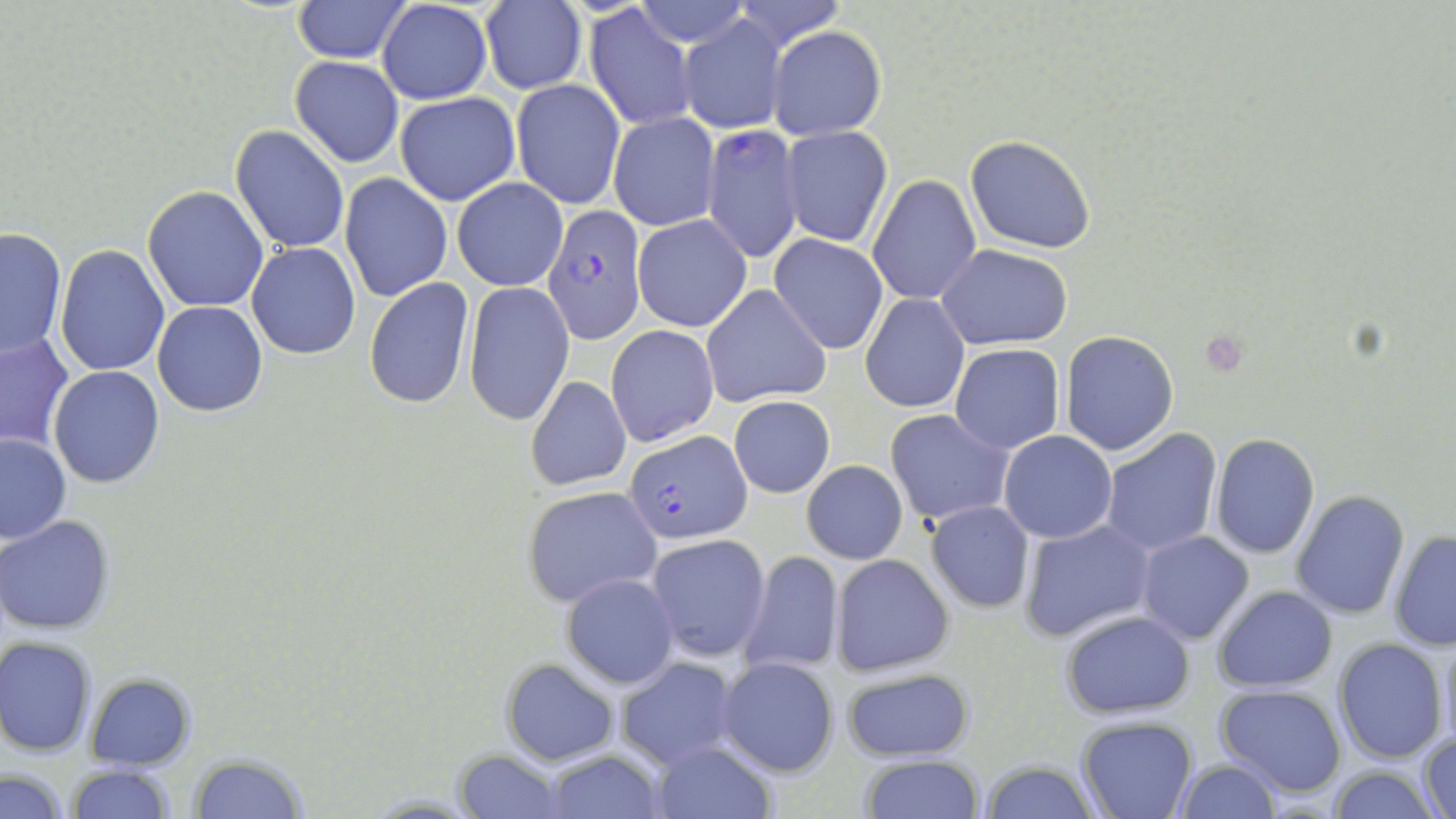
Summary:
  - Coordinate format: approximate bounding boxes as [x1, y1, x2, y2] in pixels
  - Plasmodium falciparum-infected red blood cell locations: [702, 124, 803, 262], [543, 207, 646, 340], [625, 432, 751, 543]
  - Uninfected red blood cell locations: [732, 0, 846, 52], [294, 1, 406, 62], [377, 1, 493, 104], [632, 1, 752, 47], [480, 2, 586, 94], [584, 5, 698, 131], [678, 16, 788, 133], [768, 26, 888, 139], [289, 55, 404, 167], [511, 79, 625, 209], [394, 92, 520, 206], [608, 112, 719, 232], [230, 124, 350, 254], [780, 126, 893, 248], [965, 135, 1096, 255], [866, 154, 1066, 284], [866, 173, 980, 306], [339, 174, 452, 303], [452, 177, 567, 291], [141, 187, 269, 312], [633, 215, 753, 332], [0, 228, 67, 357], [769, 233, 889, 354], [247, 242, 360, 359], [937, 244, 1074, 348], [55, 245, 170, 377], [364, 278, 477, 409], [462, 285, 574, 425], [701, 285, 831, 408], [860, 293, 970, 415], [153, 301, 268, 416], [605, 325, 719, 448], [1062, 330, 1180, 456], [0, 332, 74, 450], [950, 343, 1064, 454], [48, 366, 164, 488], [526, 375, 632, 492], [729, 395, 835, 497], [885, 408, 1014, 529], [1100, 428, 1221, 557], [1000, 431, 1117, 543], [0, 433, 72, 544], [1210, 435, 1320, 557], [801, 460, 908, 565], [522, 485, 661, 608], [1291, 490, 1410, 619], [926, 503, 1034, 612], [0, 515, 117, 636], [1019, 520, 1157, 644], [1387, 529, 1456, 650], [1136, 530, 1254, 644], [648, 534, 771, 664], [738, 549, 845, 677], [831, 555, 955, 678], [562, 573, 679, 688], [1213, 586, 1337, 692], [1059, 609, 1195, 719], [1437, 627, 1456, 754], [0, 637, 97, 755], [1333, 638, 1449, 763], [717, 656, 840, 778], [615, 657, 741, 770], [500, 658, 618, 766], [838, 664, 975, 763], [84, 672, 195, 770], [1214, 681, 1348, 798], [1076, 715, 1197, 818], [1417, 731, 1455, 817], [648, 740, 778, 818], [543, 749, 666, 818], [452, 750, 569, 819], [188, 756, 311, 817], [859, 756, 986, 817], [978, 758, 1100, 819], [1172, 761, 1283, 818], [64, 763, 176, 819], [1326, 763, 1441, 819], [2, 768, 70, 819]
  - Platelet locations: [1198, 332, 1251, 377]
  - Slide-level diagnosis: Plasmodium falciparum
  - Modality: optical microscopy
  - Stain: May-Grünwald-Giemsa
  - Field of view: single
  - Magnification: 1000x
  - Image size: 1456×819 pixels
  - Preparation: thin blood film